Locate every blood parasite and identify its species.
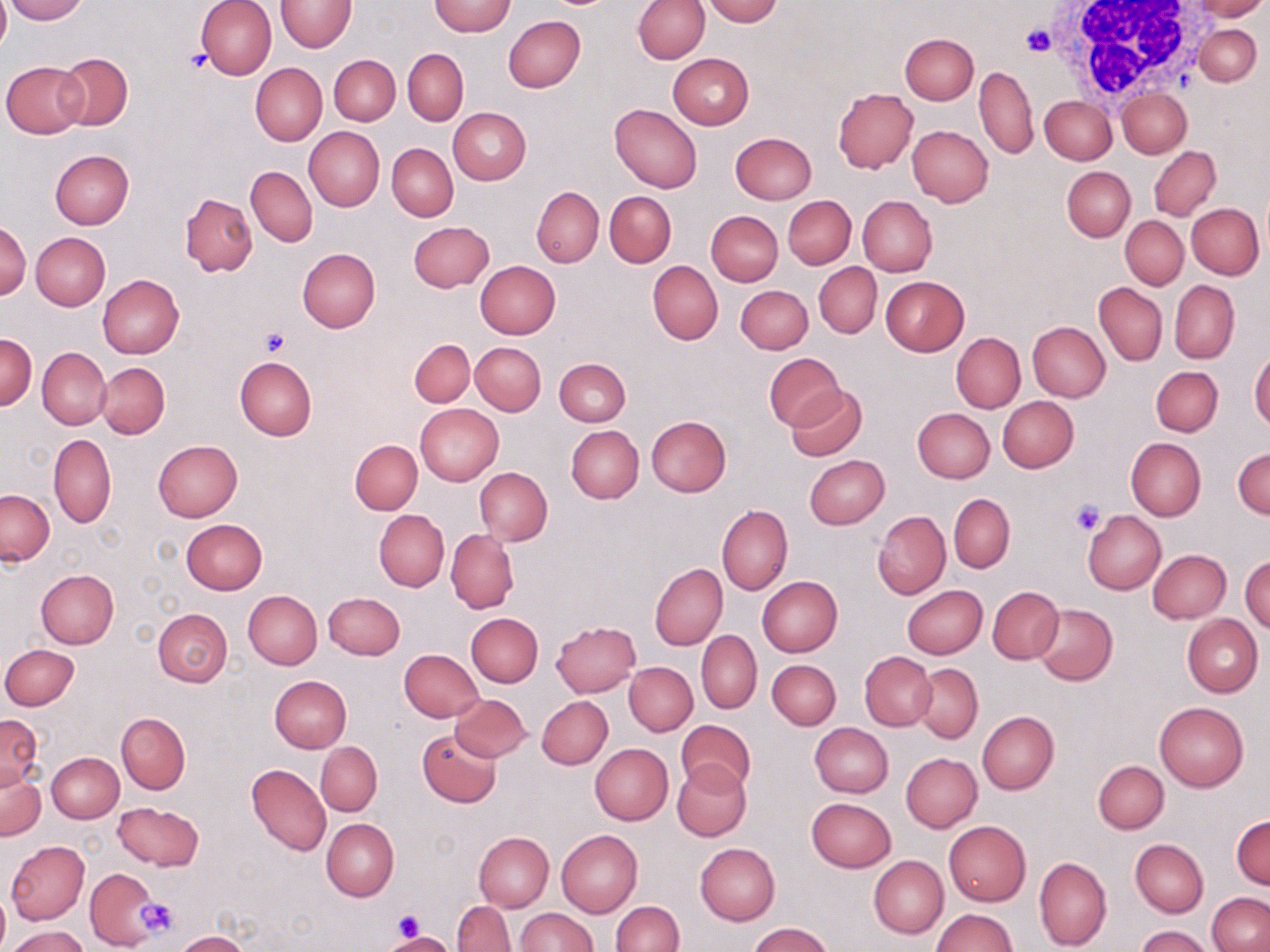

No blood parasites seen.

{
  "slide_level_diagnosis": "negative for blood parasites",
  "white_blood_cell_locations": "approximate bounding boxes as [x1, y1, x2, y2] in pixels: [1047, 0, 1205, 102]",
  "platelet_locations": "approximate bounding boxes as [x1, y1, x2, y2] in pixels: [1020, 26, 1053, 58], [181, 50, 212, 74], [258, 329, 289, 357], [1070, 500, 1104, 535], [136, 897, 180, 939], [392, 908, 425, 942]",
  "stain": "May-Grünwald-Giemsa",
  "uninfected_red_blood_cell_locations": "approximate bounding boxes as [x1, y1, x2, y2] in pixels: [0, 0, 9, 54], [4, 0, 86, 23], [195, 0, 276, 80], [275, 0, 354, 52], [633, 0, 709, 63], [703, 0, 781, 25], [1189, 0, 1267, 20], [430, 1, 515, 36], [503, 15, 585, 92], [1194, 24, 1262, 86], [900, 33, 979, 104], [402, 48, 468, 125], [55, 53, 133, 131], [667, 53, 753, 129], [330, 55, 399, 125], [2, 60, 88, 138], [250, 63, 327, 145], [974, 66, 1037, 160], [1117, 88, 1191, 157], [834, 89, 917, 173], [1039, 96, 1116, 165], [609, 104, 702, 193], [448, 107, 531, 185], [908, 125, 992, 207], [304, 127, 384, 211], [730, 133, 816, 204], [387, 143, 458, 221], [1149, 147, 1220, 221], [50, 149, 133, 229], [245, 166, 318, 247], [1062, 166, 1136, 241], [532, 186, 604, 267], [604, 191, 675, 267], [180, 193, 257, 277], [858, 195, 937, 277], [783, 196, 856, 269], [1187, 204, 1264, 279], [706, 211, 782, 286], [1120, 216, 1188, 289], [1, 220, 30, 301], [408, 221, 493, 292], [31, 233, 110, 311], [297, 247, 379, 333], [648, 260, 723, 344], [474, 261, 560, 338], [814, 262, 881, 338], [98, 275, 184, 358], [881, 275, 969, 355], [1168, 280, 1240, 364], [1094, 282, 1168, 365], [735, 285, 812, 353], [1027, 321, 1110, 402], [951, 332, 1025, 413], [2, 335, 36, 409], [409, 338, 475, 407], [470, 342, 545, 414], [37, 347, 110, 429], [1249, 349, 1270, 431], [764, 352, 843, 429], [234, 356, 316, 442], [553, 358, 631, 427], [96, 363, 170, 437], [1151, 367, 1222, 437], [785, 385, 866, 462], [996, 396, 1079, 472], [416, 404, 504, 484], [913, 407, 995, 482], [645, 415, 731, 497], [566, 426, 643, 502], [48, 433, 116, 528], [1126, 438, 1205, 522], [153, 439, 242, 522], [350, 439, 422, 515], [1233, 446, 1270, 519], [804, 454, 888, 528], [475, 467, 552, 544], [1, 490, 54, 566], [949, 494, 1015, 572], [717, 504, 794, 595], [872, 509, 950, 600], [374, 510, 448, 591], [1083, 511, 1167, 594], [181, 519, 267, 594], [446, 529, 518, 614], [1148, 548, 1231, 623], [1241, 556, 1270, 634], [650, 563, 727, 650], [36, 569, 118, 649], [756, 576, 842, 657], [901, 584, 987, 658], [988, 587, 1064, 663], [242, 590, 322, 669], [322, 592, 405, 660], [1033, 604, 1117, 685], [153, 609, 232, 686], [466, 613, 542, 687], [1182, 615, 1262, 697], [551, 620, 640, 697], [696, 630, 762, 713], [1, 644, 79, 709], [400, 649, 484, 721], [860, 652, 937, 729], [768, 659, 840, 729], [625, 661, 698, 736], [913, 663, 983, 743], [269, 676, 351, 753], [449, 694, 531, 760], [537, 696, 613, 770], [1154, 701, 1249, 791], [977, 712, 1059, 794], [0, 713, 43, 788], [117, 713, 190, 793], [677, 719, 756, 795], [809, 722, 892, 796], [418, 729, 502, 807], [315, 742, 382, 816], [590, 744, 672, 825], [46, 752, 124, 822], [901, 753, 982, 831], [1093, 760, 1168, 833], [671, 761, 751, 841], [247, 764, 331, 856], [0, 766, 44, 841], [806, 797, 897, 872], [114, 801, 203, 869], [1231, 815, 1269, 889], [322, 818, 398, 900], [944, 820, 1031, 906], [557, 829, 642, 917], [474, 831, 554, 911], [1130, 839, 1208, 917], [6, 840, 89, 924], [695, 843, 780, 925], [869, 855, 948, 938], [1034, 856, 1112, 952], [86, 869, 163, 949], [0, 888, 9, 952], [1207, 892, 1270, 952], [453, 900, 515, 951], [611, 901, 683, 952], [515, 907, 598, 951], [931, 909, 1019, 952], [749, 923, 834, 952], [8, 926, 89, 952], [1136, 926, 1214, 952], [176, 931, 248, 952], [384, 933, 453, 952]",
  "magnification": "1000x",
  "image_size": "1270×952 pixels",
  "preparation": "thin blood smear",
  "field_of_view": "one of a larger specimen",
  "modality": "optical microscopy"
}